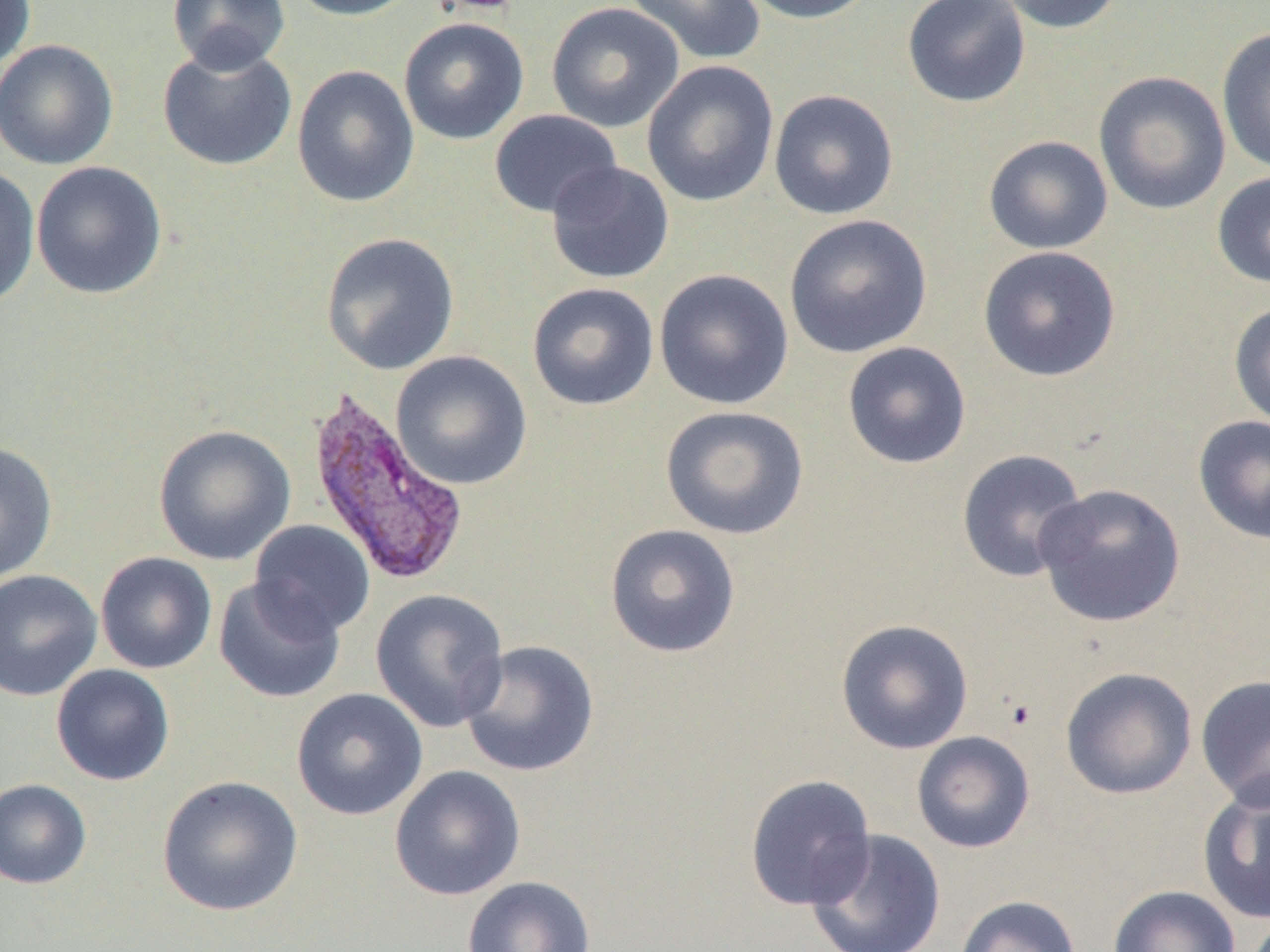

Summary:
  - Coordinate format: approximate bounding boxes as (x1,y1)-(x2,y2) corner pairs in pixels
  - Platelet locations: (432,0)-(524,15)
  - Uninfected red blood cell locations: (0,0)-(35,73), (167,0)-(290,74), (284,0)-(422,21), (422,0)-(527,16), (623,0)-(766,65), (737,0)-(879,25), (902,0)-(1031,108), (990,0)-(1126,35), (546,2)-(685,133), (398,17)-(529,145), (1216,26)-(1270,175), (0,39)-(119,170), (157,42)-(297,172), (641,60)-(779,207), (291,64)-(420,208), (1093,70)-(1232,216), (768,89)-(899,221), (489,109)-(623,219), (983,135)-(1113,254), (31,161)-(168,299), (544,161)-(675,285), (0,165)-(41,309), (1212,171)-(1270,289), (784,214)-(932,358), (319,232)-(460,375), (977,245)-(1121,382), (653,267)-(794,410), (526,282)-(660,411), (1228,301)-(1270,430), (842,341)-(972,469), (390,350)-(533,491), (660,405)-(810,540), (1192,415)-(1270,545), (153,424)-(297,566), (0,441)-(58,584), (955,449)-(1089,583), (1034,483)-(1186,628), (248,520)-(376,637), (604,523)-(741,659), (95,552)-(217,674), (0,569)-(102,701), (213,578)-(346,703), (370,589)-(509,733), (835,618)-(974,755), (458,640)-(600,778), (51,664)-(175,786), (1060,666)-(1197,799), (1195,674)-(1270,810), (291,688)-(428,821), (911,731)-(1035,853), (389,764)-(526,901), (156,774)-(304,917), (744,774)-(877,911), (0,778)-(91,889), (1196,779)-(1270,926), (806,829)-(946,952), (461,876)-(596,952), (1107,885)-(1241,952), (955,894)-(1082,952)
  - Plasmodium vivax-infected red blood cell locations: (304,388)-(468,587)
  - Slide-level diagnosis: Plasmodium vivax
  - Image size: 1270×952 pixels
  - Field of view: one of a larger specimen
  - Preparation: thin blood smear
  - Modality: optical microscopy
  - Magnification: 1000x